Assess this cell for malaria.
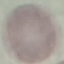
It is uninfected.

Summary:
  - Stain: Giemsa
  - Image type: cell patch, automatically extracted from a larger field of view and resized to 64 × 64 pixels
  - Preparation: thin blood smear
  - Capture: smartphone through the microscope eyepiece